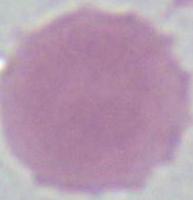
Summary:
  - Magnification: 1000x
  - Identification: red blood cell
  - Modality: photomicrograph